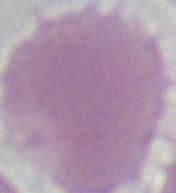

magnification = 1000x
modality = micrograph
identification = red blood cell